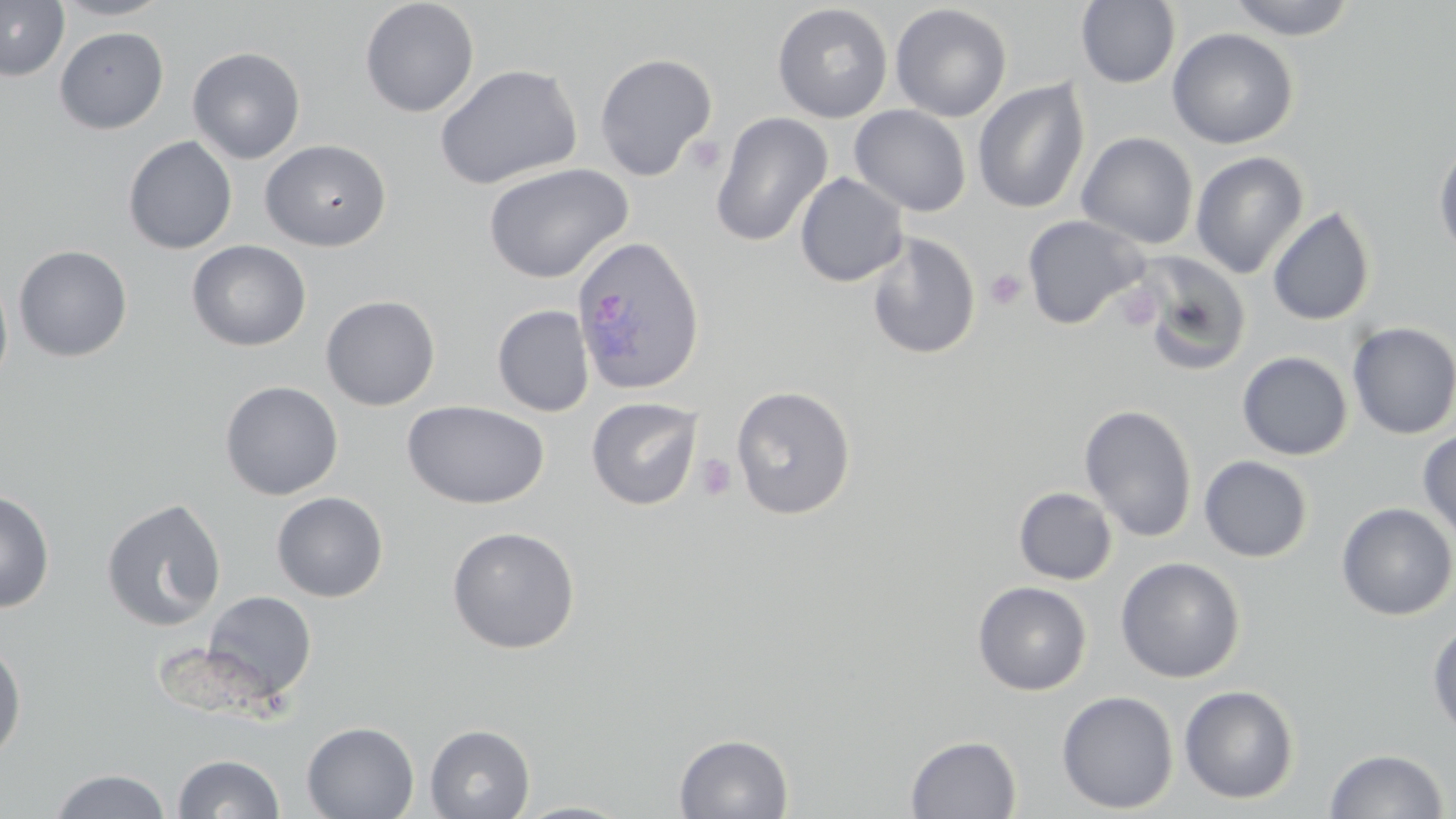

Summary:
  - Coordinate format: approximate bounding boxes as named x1/y1/x2/y2 corners in pixels
  - Platelet locations: (x1=685, y1=135, x2=725, y2=176), (x1=985, y1=268, x2=1027, y2=310), (x1=1117, y1=284, x2=1161, y2=332), (x1=695, y1=454, x2=738, y2=502)
  - Plasmodium ovale-infected red blood cell locations: (x1=570, y1=235, x2=706, y2=397)
  - Uninfected red blood cell locations: (x1=0, y1=0, x2=69, y2=81), (x1=52, y1=0, x2=171, y2=20), (x1=360, y1=0, x2=480, y2=117), (x1=1226, y1=0, x2=1358, y2=41), (x1=1076, y1=1, x2=1181, y2=89), (x1=772, y1=3, x2=893, y2=123), (x1=890, y1=4, x2=1012, y2=122), (x1=54, y1=26, x2=169, y2=134), (x1=1167, y1=27, x2=1300, y2=150), (x1=187, y1=46, x2=306, y2=164), (x1=594, y1=53, x2=718, y2=181), (x1=434, y1=63, x2=583, y2=190), (x1=972, y1=79, x2=1090, y2=215), (x1=849, y1=105, x2=972, y2=217), (x1=710, y1=111, x2=833, y2=247), (x1=1076, y1=132, x2=1199, y2=250), (x1=123, y1=135, x2=238, y2=254), (x1=1432, y1=136, x2=1456, y2=261), (x1=260, y1=139, x2=392, y2=252), (x1=1191, y1=151, x2=1309, y2=279), (x1=483, y1=162, x2=633, y2=284), (x1=794, y1=172, x2=909, y2=287), (x1=1267, y1=206, x2=1376, y2=326), (x1=1022, y1=214, x2=1149, y2=330), (x1=865, y1=231, x2=981, y2=359), (x1=186, y1=239, x2=312, y2=352), (x1=13, y1=244, x2=133, y2=362), (x1=1131, y1=250, x2=1252, y2=377), (x1=0, y1=270, x2=14, y2=394), (x1=320, y1=295, x2=440, y2=411), (x1=492, y1=304, x2=594, y2=417), (x1=1346, y1=322, x2=1456, y2=440), (x1=1237, y1=351, x2=1353, y2=460), (x1=219, y1=380, x2=344, y2=500), (x1=731, y1=385, x2=856, y2=520), (x1=586, y1=396, x2=703, y2=510), (x1=403, y1=400, x2=550, y2=510), (x1=1079, y1=403, x2=1198, y2=542), (x1=1418, y1=429, x2=1456, y2=543), (x1=1198, y1=455, x2=1313, y2=563), (x1=1013, y1=487, x2=1118, y2=585), (x1=0, y1=488, x2=56, y2=613), (x1=271, y1=491, x2=389, y2=602), (x1=100, y1=497, x2=227, y2=632), (x1=1336, y1=502, x2=1456, y2=621), (x1=446, y1=525, x2=580, y2=654), (x1=1115, y1=556, x2=1246, y2=683), (x1=973, y1=581, x2=1092, y2=696), (x1=201, y1=590, x2=317, y2=702), (x1=1427, y1=621, x2=1456, y2=739), (x1=0, y1=637, x2=27, y2=764), (x1=1179, y1=684, x2=1300, y2=805), (x1=1056, y1=690, x2=1179, y2=814), (x1=301, y1=721, x2=419, y2=819), (x1=425, y1=724, x2=535, y2=819), (x1=673, y1=733, x2=794, y2=818), (x1=905, y1=735, x2=1022, y2=818), (x1=1325, y1=748, x2=1449, y2=818), (x1=172, y1=753, x2=285, y2=818), (x1=49, y1=769, x2=172, y2=818), (x1=510, y1=800, x2=637, y2=819)
  - Slide-level diagnosis: Plasmodium ovale
  - Field of view: single
  - Modality: light microscopy
  - Magnification: 1000x
  - Preparation: thin blood smear
  - Image size: 1456×819 pixels
  - Stain: May-Grünwald-Giemsa